Describe the morphology of the erythrocytes.
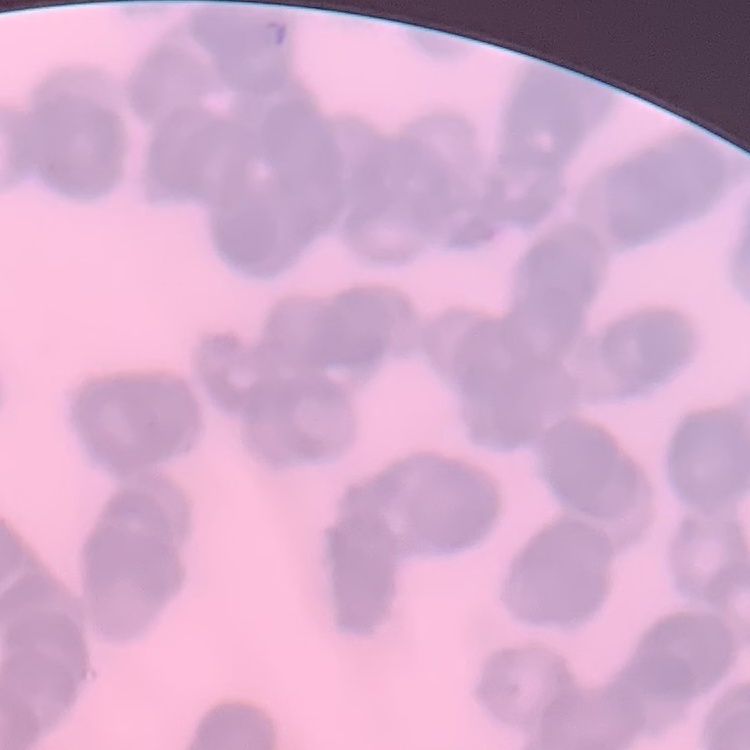

They show rouleaux formation.

One tile cut from a larger photomicrograph. Field's or Giemsa stain. Thin peripheral smear.